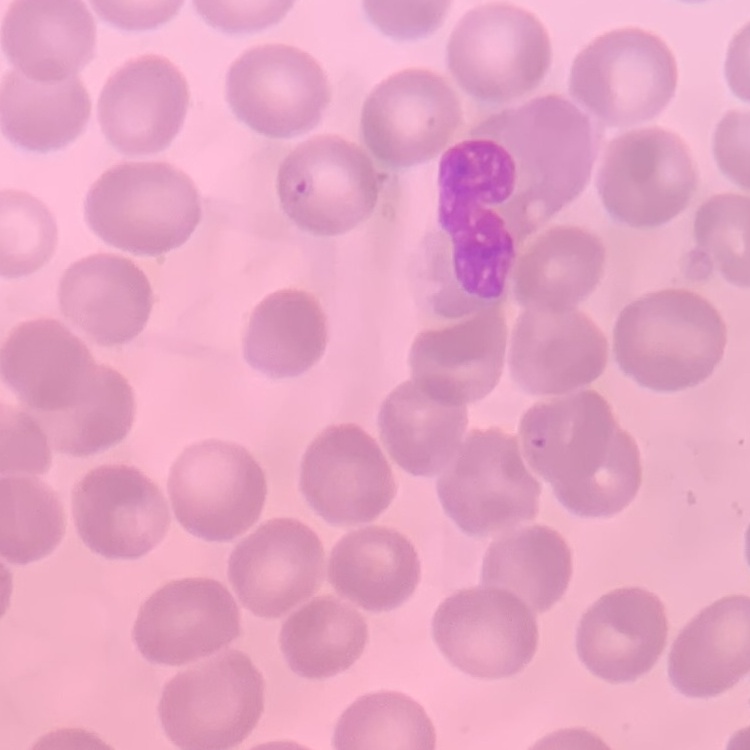 The red blood cells show no rouleaux formation. Stained with either Field's or Giemsa. Thin peripheral smear. One tile cut from a larger photomicrograph.